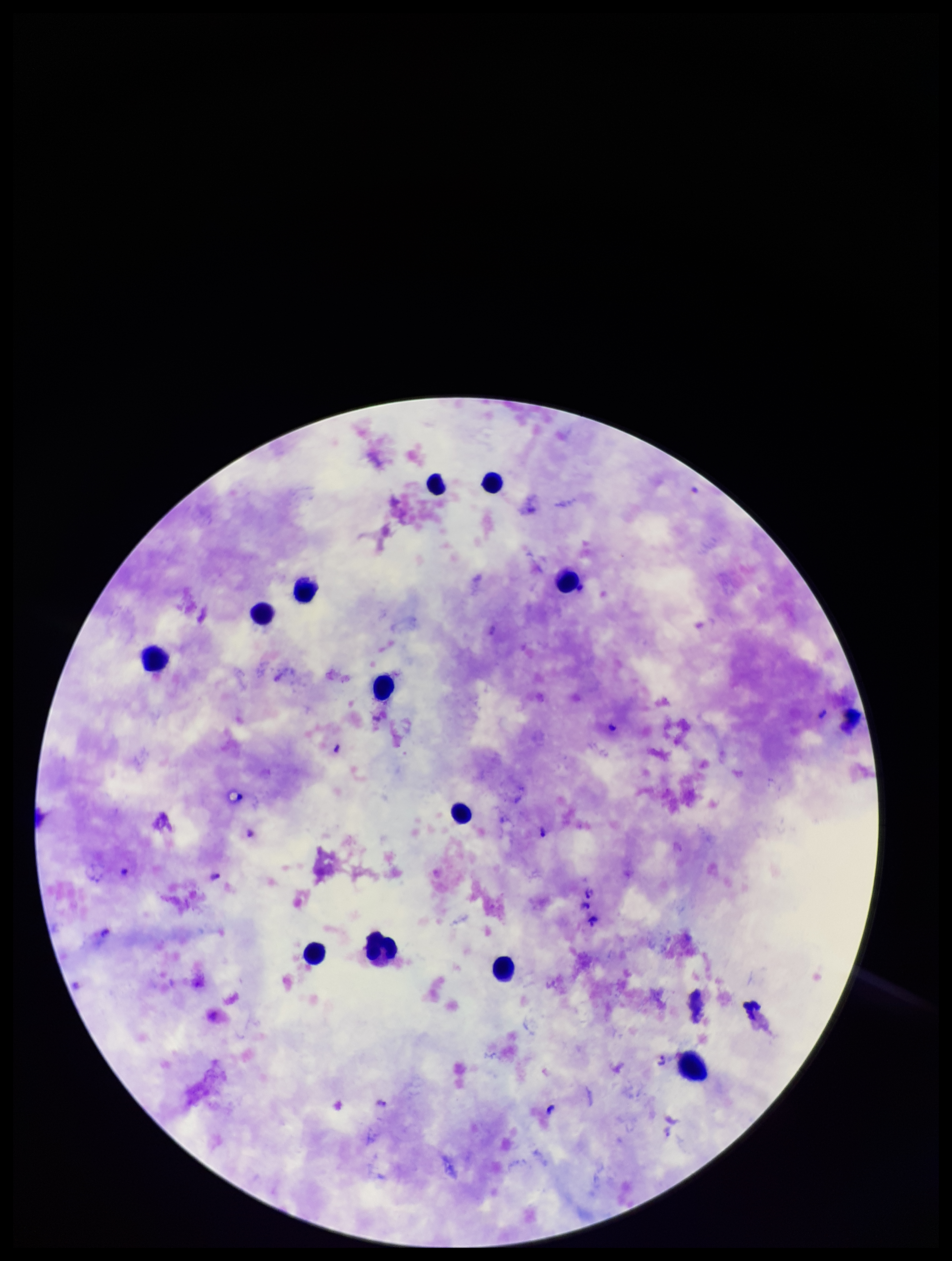
Giemsa stain. Leukocyte count: 12. Preparation: thick blood smear. Patient malaria status: infected. Single field of view. Photographed through the microscope eyepiece with a smartphone camera. Parasite count: 11. Species reported for this patient: Plasmodium falciparum. Image is 952×1261 pixels. Plasmodium parasites: seen.